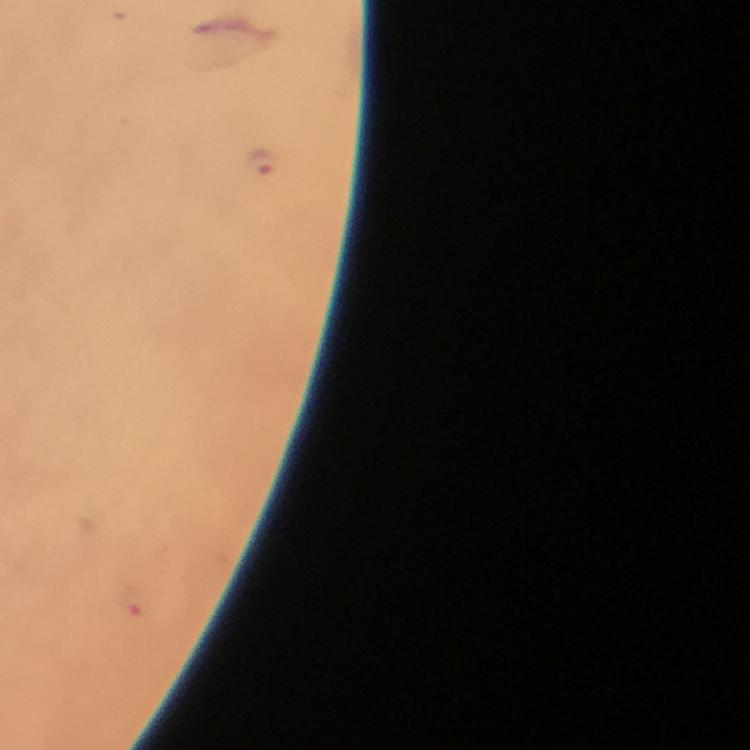 Approximate centers as [x, y] in pixels. Plasmodium parasite locations: [262, 162]. Thick blood smear. 100x magnification. Image is 750×750 pixels. From a malaria diagnostic workup. Giemsa-stained preparation. Smartphone photograph taken through a microscope. A crop from one field of view. Immersion oil applied.